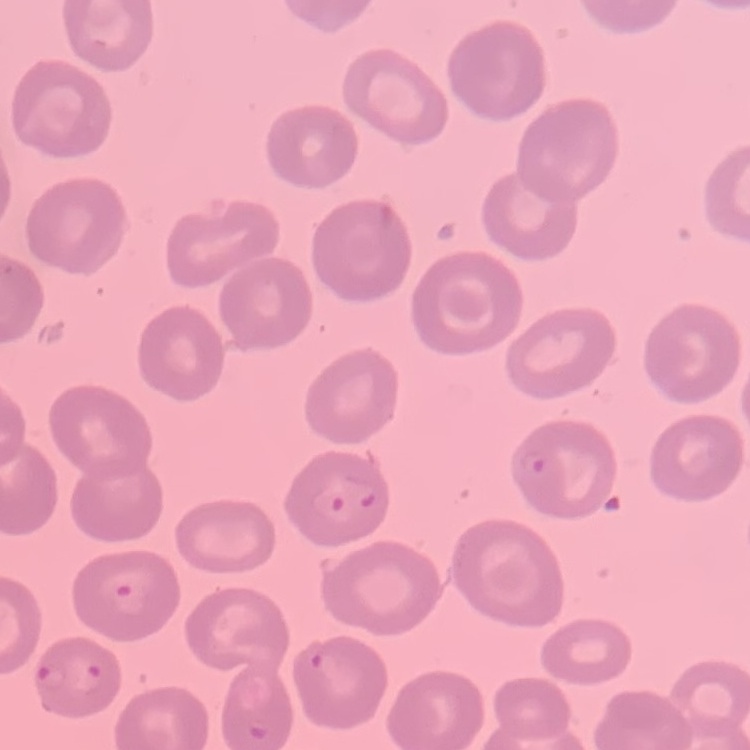 The erythrocytes exhibit no rouleaux formation. Thin peripheral smear. Field's or Giemsa stain. One tile cut from a larger photomicrograph.